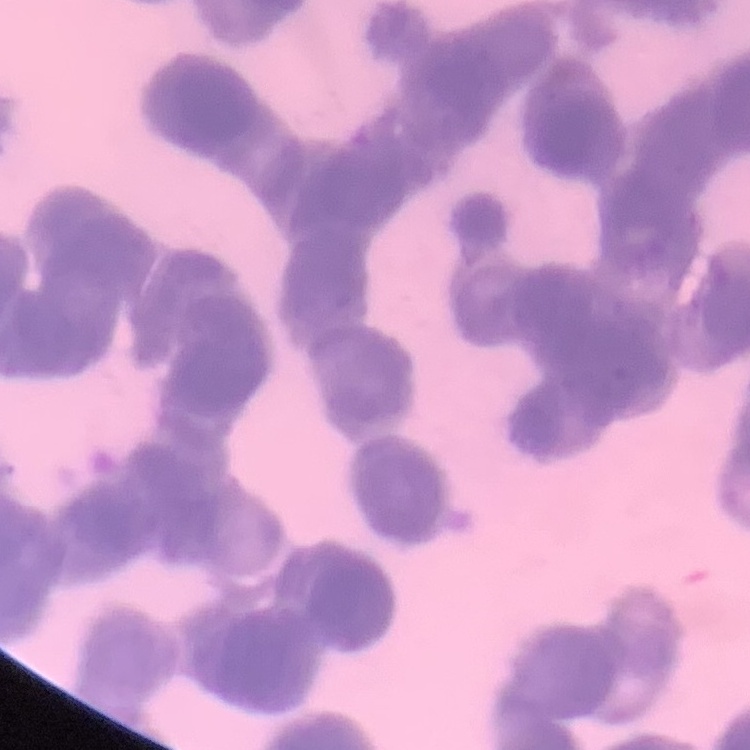
Summary:
  - Red blood cell morphology: rouleaux formation
  - Image type: one tile cut from a larger photomicrograph
  - Preparation: thin blood smear
  - Stain: Field's or Giemsa